Assess this cell for malaria.
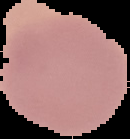

It is uninfected.

Segmented cell region on a black background. Image is 130×139 pixels. From a thin blood film.